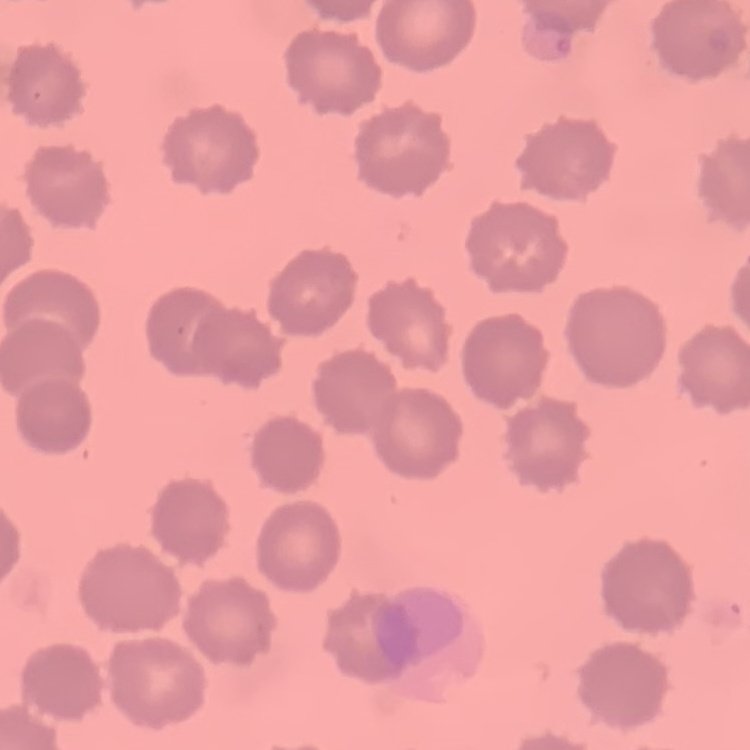

red blood cell morphology = no rouleaux formation
preparation = thin blood film
stain = Field's or Giemsa
image type = square crop of a larger photomicrograph